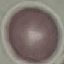
Summary:
  - Result: no malaria parasites detected
  - Image type: automatically extracted cell patch, resized to 64 × 64 pixels
  - Stain: Giemsa
  - Preparation: thin smear
  - Capture: smartphone camera at the microscope eyepiece